Outline each blood parasite and name the species.
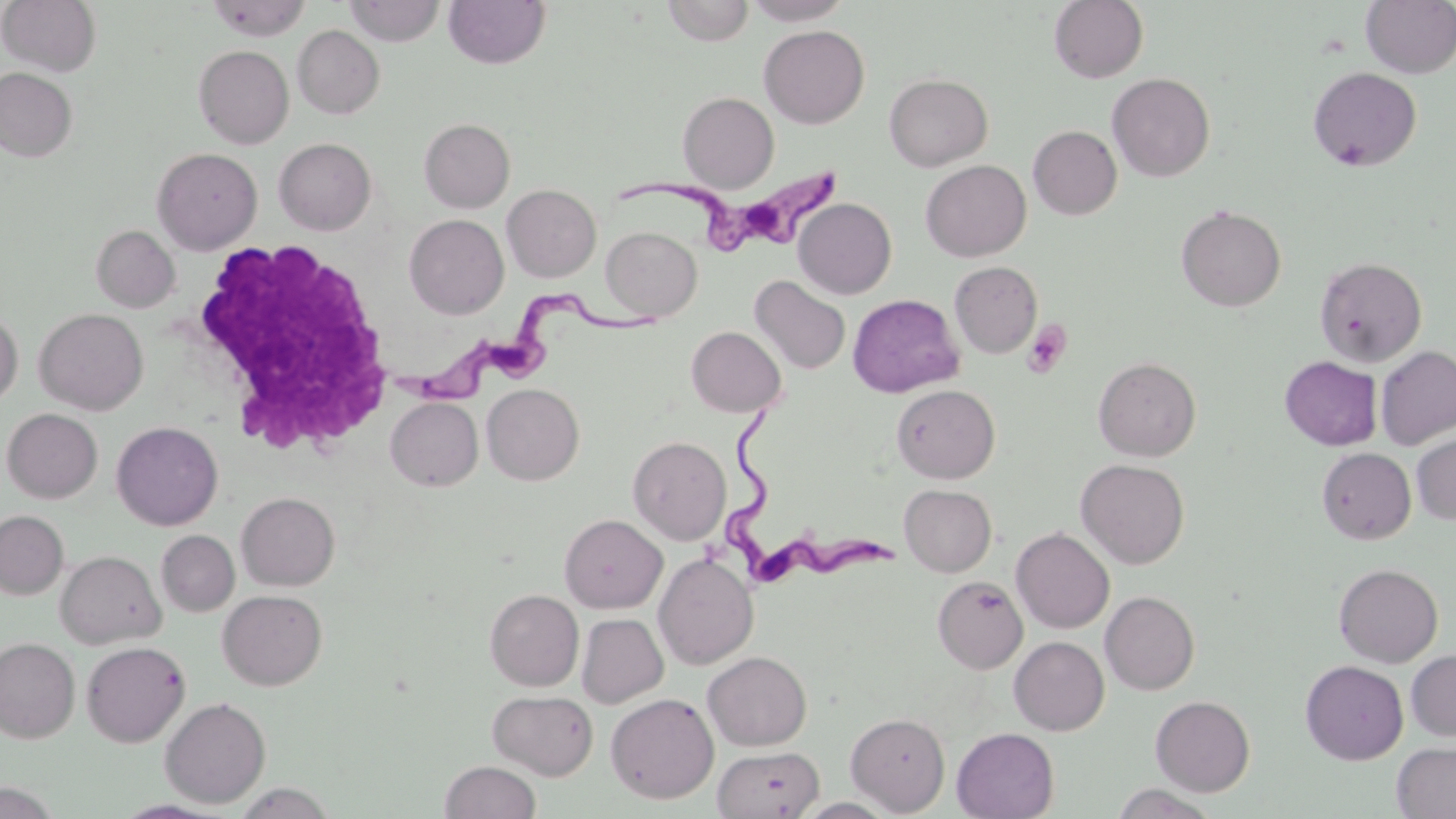
Approximate bounding boxes as (x1,y1)-(x2,y2) corner pairs in pixels.
Trypanosoma brucei: (619,152)-(845,259), (402,285)-(669,403), (711,406)-(894,584).
No Plasmodium falciparum, Plasmodium ovale, Plasmodium malariae, Plasmodium vivax, or Babesia divergens observed.

Summary:
  - Uninfected red blood cell locations: (0,0)-(101,76), (207,0)-(311,41), (661,0)-(754,45), (743,0)-(853,25), (1049,0)-(1148,83), (1360,0)-(1456,78), (344,1)-(445,46), (443,1)-(550,70), (292,25)-(384,119), (759,25)-(870,128), (194,45)-(294,149), (1307,66)-(1423,171), (0,67)-(77,162), (884,73)-(993,171), (1108,73)-(1215,182), (677,92)-(779,192), (419,118)-(515,212), (1028,125)-(1122,219), (274,138)-(376,235), (152,147)-(262,254), (921,160)-(1031,261), (502,184)-(601,282), (793,198)-(897,299), (1176,204)-(1287,312), (404,214)-(509,319), (92,225)-(180,312), (601,226)-(702,320), (1314,256)-(1427,367), (949,261)-(1043,358), (750,275)-(851,374), (847,294)-(963,398), (34,308)-(149,415), (0,310)-(22,408), (687,326)-(786,417), (1375,345)-(1456,450), (1093,356)-(1201,461), (1280,356)-(1382,450), (482,383)-(584,485), (890,384)-(1000,483), (386,397)-(483,491), (2,408)-(102,503), (2,411)-(223,514), (111,421)-(223,531), (1411,430)-(1456,524), (628,435)-(731,545), (1317,447)-(1416,544), (1076,459)-(1190,569), (899,484)-(997,576), (237,492)-(339,591), (0,510)-(68,599), (559,514)-(667,613), (1011,528)-(1114,633), (156,530)-(240,616), (55,550)-(165,648), (654,552)-(758,669), (1333,563)-(1443,667), (933,576)-(1028,674), (485,589)-(584,691), (217,590)-(327,690), (1100,591)-(1200,694), (577,613)-(668,708), (1009,636)-(1109,735), (0,637)-(80,743), (81,641)-(190,747), (1406,649)-(1456,741), (703,651)-(812,750), (1300,660)-(1408,764), (488,689)-(598,780), (606,692)-(719,803), (1151,695)-(1255,796), (160,697)-(271,807), (846,712)-(950,815), (952,727)-(1059,818), (1392,742)-(1456,818), (713,745)-(823,819), (440,760)-(541,819), (0,780)-(64,818), (234,782)-(338,819)
  - White blood cell locations: (180,236)-(395,457)
  - Platelet locations: (1022,320)-(1073,378)
  - Slide-level diagnosis: Trypanosoma brucei
  - Modality: optical microscopy
  - Magnification: 1000x
  - Image size: 1456×819 pixels
  - Field of view: single
  - Preparation: thin blood film
  - Stain: May-Grünwald-Giemsa